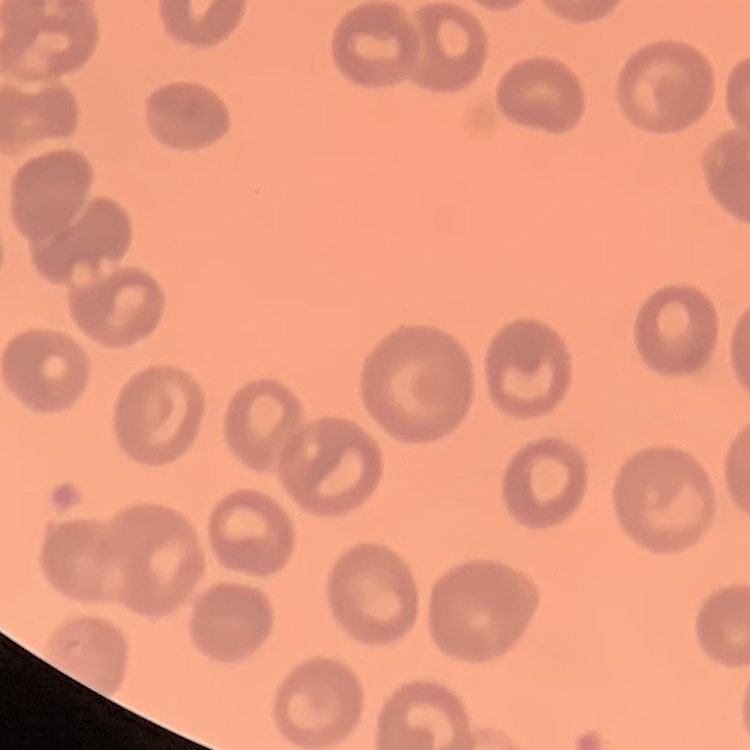
Summary:
  - Erythrocyte morphology: no rouleaux formation
  - Preparation: thin peripheral smear
  - Stain: Field's or Giemsa
  - Image type: square crop of a larger photomicrograph